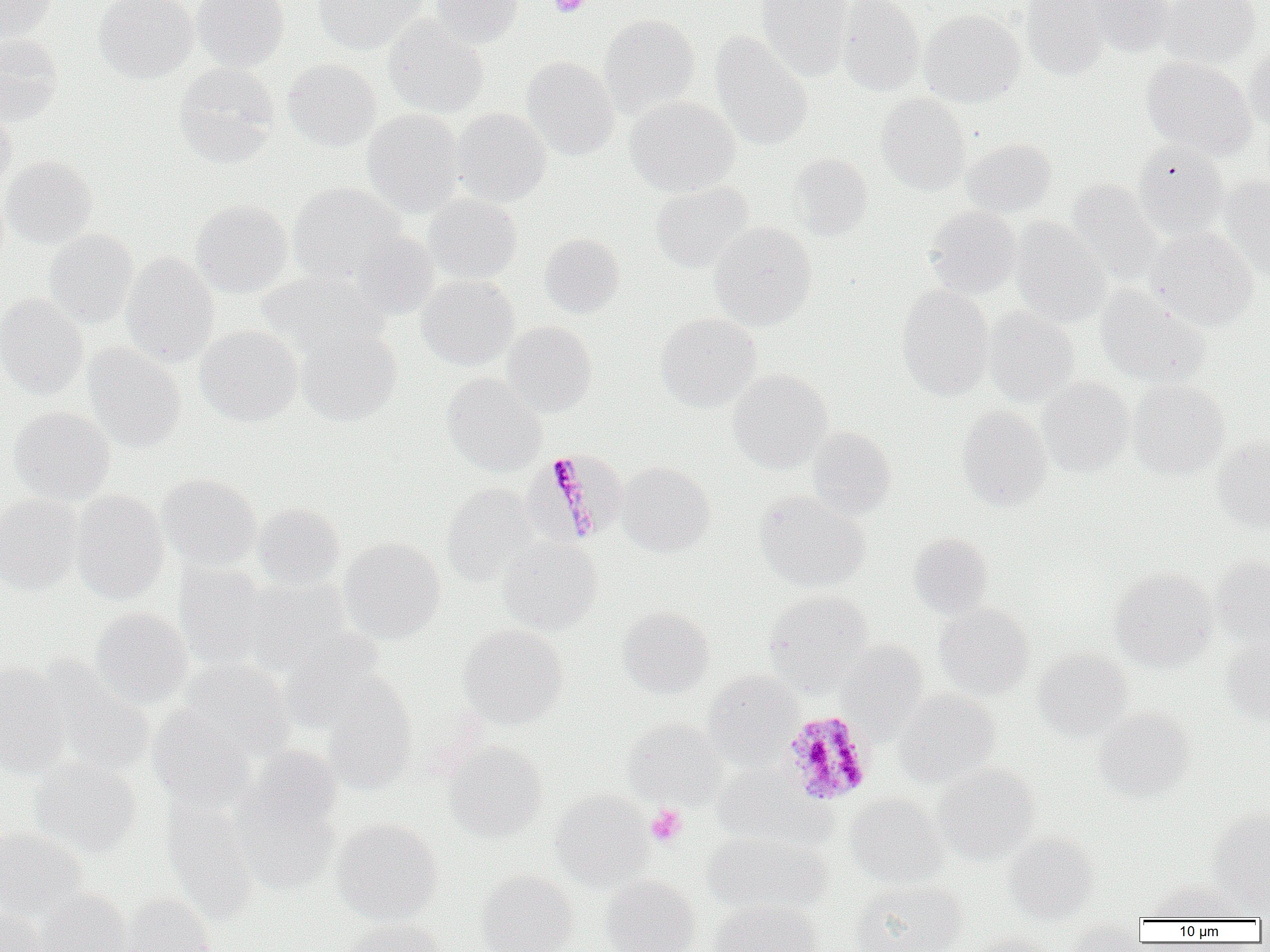

Summary:
  - Coordinate format: approximate bounding boxes as named x1/y1/x2/y2 corners in pixels
  - Plasmodium malariae-infected red blood cell locations: (x1=527, y1=449, x2=627, y2=545), (x1=780, y1=710, x2=875, y2=805)
  - Uninfected red blood cell locations: (x1=0, y1=0, x2=56, y2=40), (x1=94, y1=0, x2=197, y2=82), (x1=192, y1=0, x2=289, y2=71), (x1=313, y1=0, x2=426, y2=54), (x1=430, y1=0, x2=523, y2=48), (x1=757, y1=0, x2=854, y2=81), (x1=836, y1=0, x2=925, y2=96), (x1=1020, y1=0, x2=1109, y2=79), (x1=1079, y1=0, x2=1176, y2=57), (x1=1160, y1=0, x2=1260, y2=68), (x1=919, y1=8, x2=1025, y2=106), (x1=599, y1=14, x2=700, y2=117), (x1=383, y1=18, x2=489, y2=118), (x1=710, y1=33, x2=813, y2=150), (x1=0, y1=34, x2=63, y2=124), (x1=1244, y1=44, x2=1270, y2=130), (x1=1142, y1=55, x2=1257, y2=160), (x1=521, y1=56, x2=619, y2=160), (x1=282, y1=58, x2=380, y2=152), (x1=174, y1=62, x2=280, y2=168), (x1=876, y1=93, x2=971, y2=194), (x1=626, y1=96, x2=740, y2=196), (x1=0, y1=108, x2=17, y2=192), (x1=362, y1=108, x2=464, y2=217), (x1=452, y1=108, x2=551, y2=206), (x1=961, y1=137, x2=1056, y2=217), (x1=1132, y1=141, x2=1230, y2=239), (x1=788, y1=152, x2=873, y2=240), (x1=1, y1=156, x2=97, y2=248), (x1=1219, y1=176, x2=1270, y2=280), (x1=1067, y1=179, x2=1167, y2=287), (x1=651, y1=182, x2=753, y2=272), (x1=287, y1=183, x2=406, y2=285), (x1=423, y1=193, x2=522, y2=285), (x1=190, y1=199, x2=293, y2=297), (x1=925, y1=206, x2=1021, y2=298), (x1=1009, y1=217, x2=1110, y2=327), (x1=710, y1=221, x2=816, y2=329), (x1=1148, y1=226, x2=1258, y2=330), (x1=44, y1=229, x2=138, y2=328), (x1=349, y1=230, x2=439, y2=319), (x1=539, y1=233, x2=624, y2=317), (x1=121, y1=252, x2=219, y2=366), (x1=256, y1=270, x2=387, y2=357), (x1=417, y1=275, x2=518, y2=370), (x1=897, y1=285, x2=994, y2=400), (x1=1094, y1=286, x2=1209, y2=387), (x1=0, y1=293, x2=88, y2=399), (x1=983, y1=308, x2=1079, y2=406), (x1=656, y1=312, x2=760, y2=411), (x1=501, y1=321, x2=597, y2=416), (x1=195, y1=325, x2=303, y2=426), (x1=296, y1=325, x2=401, y2=425), (x1=84, y1=343, x2=185, y2=451), (x1=728, y1=370, x2=832, y2=473), (x1=442, y1=373, x2=546, y2=476), (x1=1037, y1=378, x2=1135, y2=476), (x1=1129, y1=380, x2=1230, y2=479), (x1=7, y1=405, x2=115, y2=504), (x1=956, y1=406, x2=1052, y2=510), (x1=807, y1=427, x2=897, y2=520), (x1=1211, y1=436, x2=1270, y2=531), (x1=617, y1=461, x2=714, y2=556), (x1=156, y1=473, x2=262, y2=571), (x1=441, y1=483, x2=540, y2=587), (x1=70, y1=489, x2=170, y2=603), (x1=755, y1=490, x2=869, y2=592), (x1=0, y1=494, x2=83, y2=594), (x1=253, y1=502, x2=345, y2=590), (x1=908, y1=532, x2=993, y2=620), (x1=498, y1=536, x2=601, y2=634), (x1=339, y1=537, x2=445, y2=643), (x1=1211, y1=555, x2=1270, y2=647), (x1=174, y1=562, x2=268, y2=671), (x1=1109, y1=568, x2=1217, y2=670), (x1=244, y1=577, x2=352, y2=675), (x1=763, y1=591, x2=872, y2=693), (x1=935, y1=603, x2=1034, y2=699), (x1=618, y1=606, x2=714, y2=698), (x1=91, y1=607, x2=193, y2=708), (x1=460, y1=624, x2=568, y2=728), (x1=278, y1=633, x2=388, y2=733), (x1=1222, y1=637, x2=1270, y2=727), (x1=837, y1=641, x2=927, y2=739), (x1=1033, y1=649, x2=1133, y2=740), (x1=177, y1=657, x2=296, y2=763), (x1=36, y1=660, x2=157, y2=776), (x1=0, y1=662, x2=72, y2=777), (x1=703, y1=670, x2=803, y2=765), (x1=320, y1=676, x2=418, y2=794), (x1=893, y1=689, x2=999, y2=786), (x1=147, y1=706, x2=255, y2=811), (x1=1094, y1=707, x2=1195, y2=802), (x1=623, y1=717, x2=727, y2=808), (x1=446, y1=741, x2=548, y2=840), (x1=246, y1=745, x2=342, y2=834), (x1=30, y1=758, x2=141, y2=857), (x1=934, y1=763, x2=1040, y2=863), (x1=711, y1=765, x2=818, y2=846), (x1=234, y1=789, x2=340, y2=895), (x1=550, y1=790, x2=653, y2=889), (x1=845, y1=793, x2=947, y2=889), (x1=162, y1=800, x2=259, y2=924), (x1=1208, y1=808, x2=1270, y2=910), (x1=332, y1=818, x2=443, y2=924), (x1=0, y1=826, x2=85, y2=919), (x1=702, y1=830, x2=831, y2=915), (x1=1003, y1=832, x2=1098, y2=924), (x1=477, y1=870, x2=577, y2=952), (x1=600, y1=874, x2=700, y2=952), (x1=849, y1=880, x2=966, y2=952), (x1=1144, y1=880, x2=1246, y2=921), (x1=36, y1=888, x2=134, y2=952), (x1=122, y1=894, x2=216, y2=952), (x1=708, y1=899, x2=821, y2=952), (x1=0, y1=906, x2=47, y2=952), (x1=336, y1=919, x2=444, y2=952), (x1=1064, y1=920, x2=1145, y2=952), (x1=960, y1=932, x2=1055, y2=952)
  - Platelet locations: (x1=549, y1=0, x2=590, y2=17), (x1=646, y1=805, x2=687, y2=847)
  - Slide-level diagnosis: Plasmodium malariae
  - Preparation: thin blood smear
  - Magnification: 1000x
  - Field of view: single
  - Modality: light microscopy
  - Image size: 1270×952 pixels